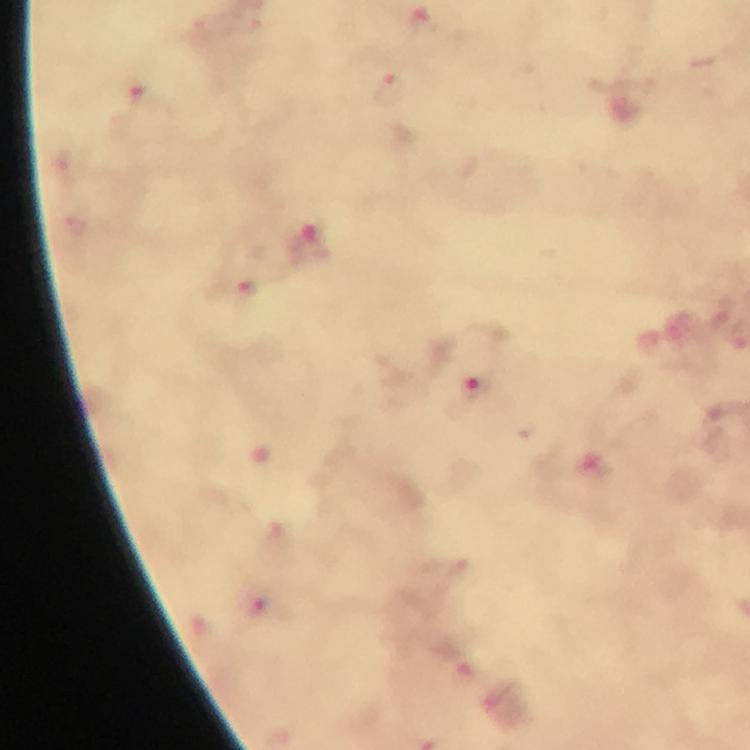

immersion oil = used
preparation = thick blood film
context = from a diagnostic examination for malaria
magnification = 100x
image size = 750×750 pixels
capture = smartphone mounted on the microscope
malaria parasite locations = approximate centers as (x, y) in pixels: (423, 21), (390, 89), (144, 94), (250, 293), (475, 389), (257, 606)
stain = Giemsa
cropped from = one field of view